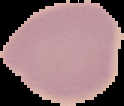
Summary:
  - Result: no malaria parasites seen
  - Image type: cell region segmented out of the field of view; surrounding area masked to black
  - Preparation: thin blood smear
  - Image size: 124×106 pixels